Locate leukocytes (white blood cells).
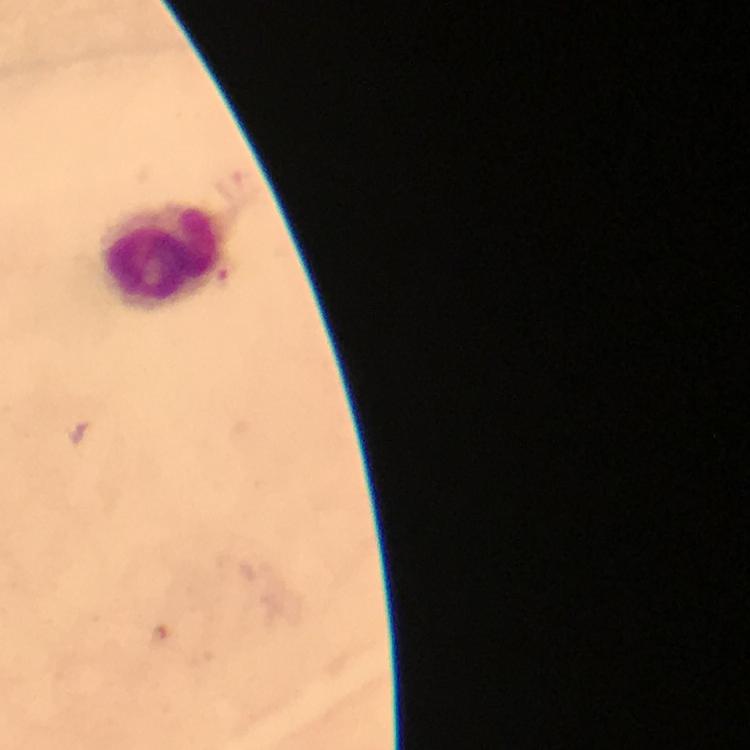
Approximate object centers, in pixels from the top-left corner.
Leukocytes: (x=161, y=256).

Malaria parasite locations: (x=79, y=432), (x=163, y=639). Cropped region of a single field of view. Immersion oil was used. Giemsa stain. Thick blood smear. Image is 750×750 pixels. Photographed through the microscope with a smartphone camera. From a malaria diagnostic workup. At 100x magnification.